Identify the cell.
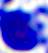

A leukocyte.

Summary:
  - Magnification: 400x
  - Modality: photomicrograph